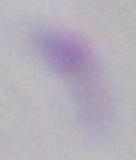
identification = Toxoplasma gondii
modality = photomicrograph
magnification = 1000x